Point out each malaria parasite and each leukocyte.
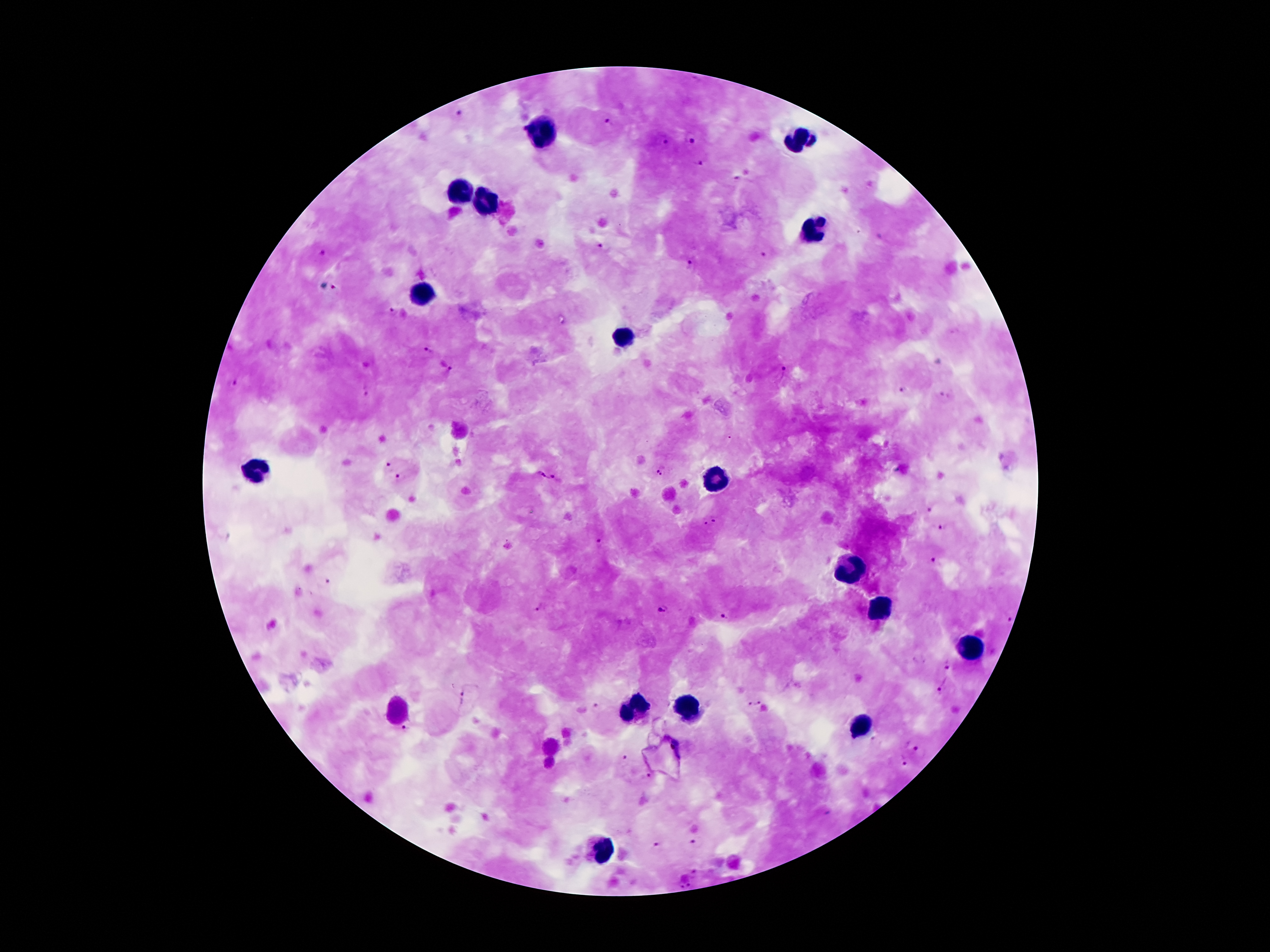
Approximate centers as [x, y] in pixels.
Malaria parasites: [457, 114], [607, 124], [693, 137], [661, 141], [697, 165], [741, 180], [603, 247], [320, 252], [770, 252], [691, 262], [335, 289], [393, 311], [428, 351], [449, 370], [780, 373], [231, 384], [367, 390], [903, 390], [943, 395], [388, 466], [658, 473], [541, 474], [554, 476], [400, 477], [927, 509], [715, 519], [704, 522], [943, 527], [602, 541], [937, 561], [326, 584], [539, 606], [661, 609], [726, 614], [1007, 618], [947, 663], [943, 683], [464, 697], [754, 701], [596, 705], [404, 729], [873, 740], [915, 749], [627, 759], [901, 760], [647, 778], [698, 841], [657, 847], [695, 874], [685, 885].
Leukocytes: [544, 133], [796, 139], [457, 193], [489, 202], [813, 230], [421, 294], [625, 336], [259, 470], [716, 479], [852, 569], [880, 609], [966, 647], [687, 706], [634, 709], [398, 711], [863, 727], [603, 852].

image_size: 1270×952 pixels
magnification: 100x
patient_malaria_status: infected with Plasmodium falciparum
stain: Giemsa
preparation: thick blood film
capture: smartphone camera through the microscope eyepiece
field_of_view: single